Identify the cell.
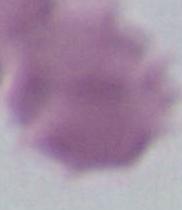

This is an erythrocyte.

1000x magnification. Photomicrograph.